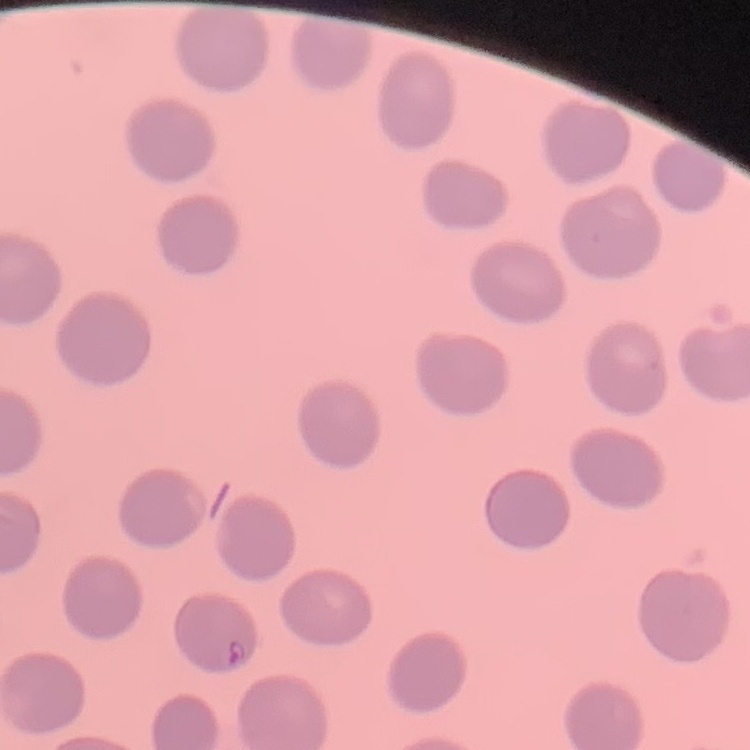

erythrocyte morphology = no rouleaux formation
preparation = thin blood smear
stain = Field's or Giemsa
image type = square crop of a larger photomicrograph